Outline each blood parasite and name the species.
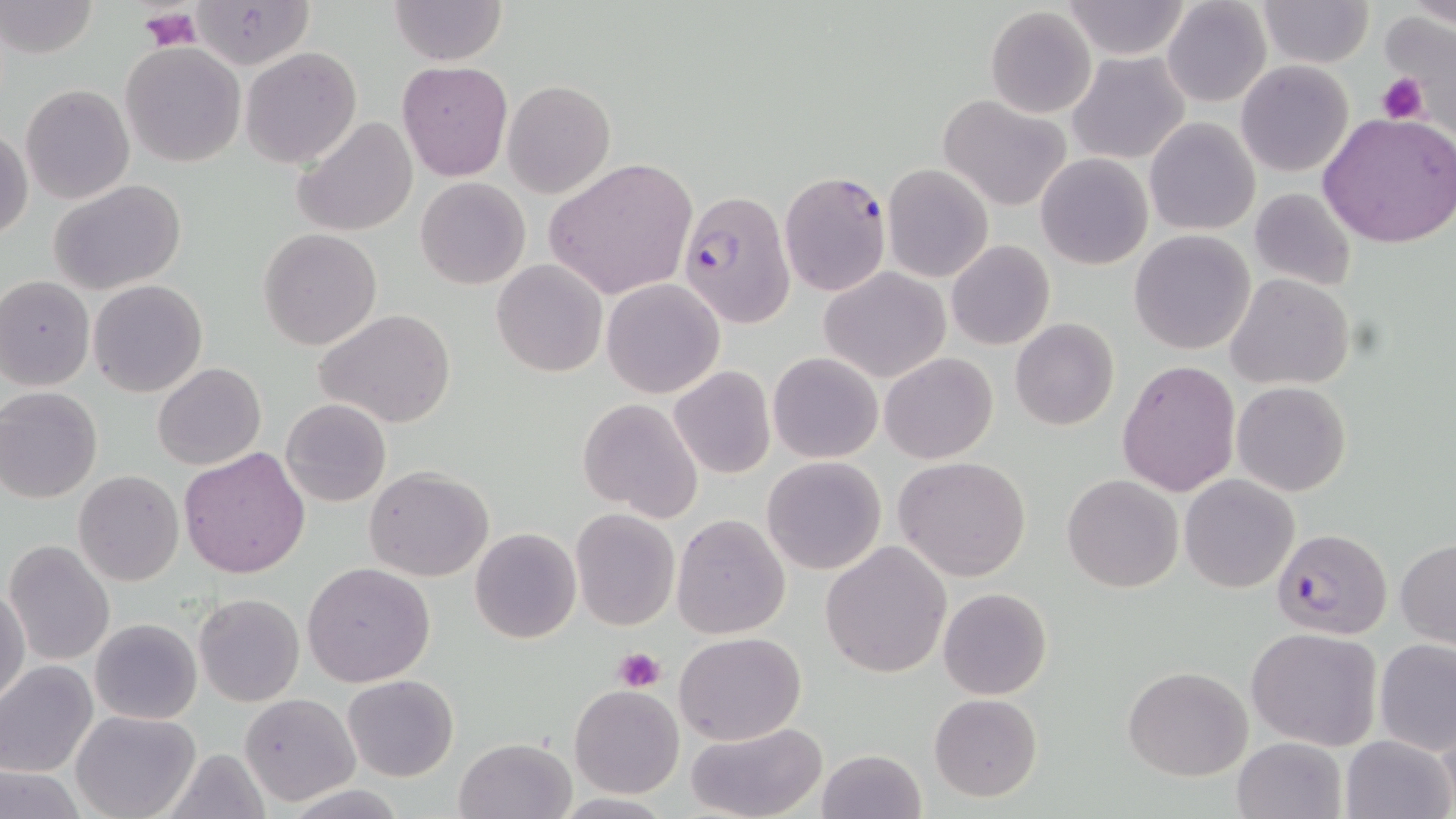
Approximate bounding boxes as [x1, y1, x2, y2] in pixels.
Plasmodium falciparum-infected red blood cells: [779, 169, 892, 297], [677, 191, 797, 325], [1272, 528, 1392, 639].
No Plasmodium ovale, Plasmodium malariae, Plasmodium vivax, Babesia divergens, or Trypanosoma brucei observed.

slide-level diagnosis = Plasmodium falciparum
preparation = thin blood film
uninfected red blood cell locations = approximate bounding boxes as [x1, y1, x2, y2] in pixels: [387, 0, 508, 67], [1161, 0, 1272, 107], [1259, 0, 1373, 69], [1, 1, 100, 58], [1062, 1, 1192, 59], [192, 2, 312, 68], [985, 6, 1096, 118], [120, 40, 247, 168], [241, 47, 361, 167], [1068, 51, 1190, 165], [397, 61, 512, 181], [1236, 61, 1353, 176], [501, 80, 615, 198], [21, 84, 134, 205], [940, 95, 1072, 211], [1318, 112, 1456, 248], [1145, 116, 1261, 236], [294, 117, 419, 237], [0, 126, 32, 243], [282, 126, 403, 332], [1036, 153, 1153, 270], [543, 158, 698, 299], [882, 166, 993, 282], [415, 176, 530, 290], [50, 180, 187, 295], [1249, 187, 1358, 292], [257, 228, 382, 350], [1128, 230, 1255, 354], [946, 240, 1055, 351], [492, 259, 608, 377], [818, 267, 949, 382], [1226, 275, 1353, 390], [0, 276, 95, 391], [601, 278, 725, 398], [88, 279, 207, 396], [0, 303, 96, 480], [316, 310, 457, 429], [1010, 319, 1120, 432], [769, 352, 883, 462], [880, 353, 998, 464], [1115, 359, 1240, 497], [152, 363, 267, 469], [669, 366, 776, 478], [1233, 382, 1351, 497], [0, 388, 102, 502], [280, 397, 391, 506], [578, 398, 704, 524], [178, 446, 311, 578], [762, 456, 887, 575], [893, 456, 1031, 581], [364, 465, 494, 582], [73, 470, 185, 586], [1062, 474, 1183, 592], [1179, 474, 1300, 592], [571, 509, 679, 629], [671, 513, 790, 639], [469, 529, 581, 644], [1397, 539, 1456, 648], [5, 541, 115, 665], [820, 541, 951, 678], [302, 562, 436, 687], [1, 582, 28, 709], [937, 587, 1053, 699], [194, 593, 305, 707], [90, 617, 202, 725], [1246, 626, 1383, 750], [674, 632, 806, 744], [1374, 640, 1456, 755], [0, 661, 98, 776], [1123, 665, 1252, 781], [342, 675, 458, 782], [569, 684, 685, 798], [239, 691, 361, 807], [930, 693, 1042, 803], [71, 710, 201, 819], [684, 722, 827, 818], [1341, 735, 1454, 819], [1233, 736, 1347, 819], [452, 737, 577, 819], [815, 749, 926, 819], [1, 765, 88, 818]
field of view = single
modality = optical microscopy
magnification = 1000x
platelet locations = approximate bounding boxes as [x1, y1, x2, y2] in pixels: [137, 5, 199, 51], [1378, 73, 1427, 126], [614, 648, 665, 692]
image size = 1456×819 pixels
stain = May-Grünwald-Giemsa